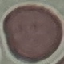

malaria status = uninfected
image type = automatically extracted cell patch, resized to 64 × 64 pixels
stain = Giemsa
capture = smartphone through the microscope eyepiece
preparation = thin smear